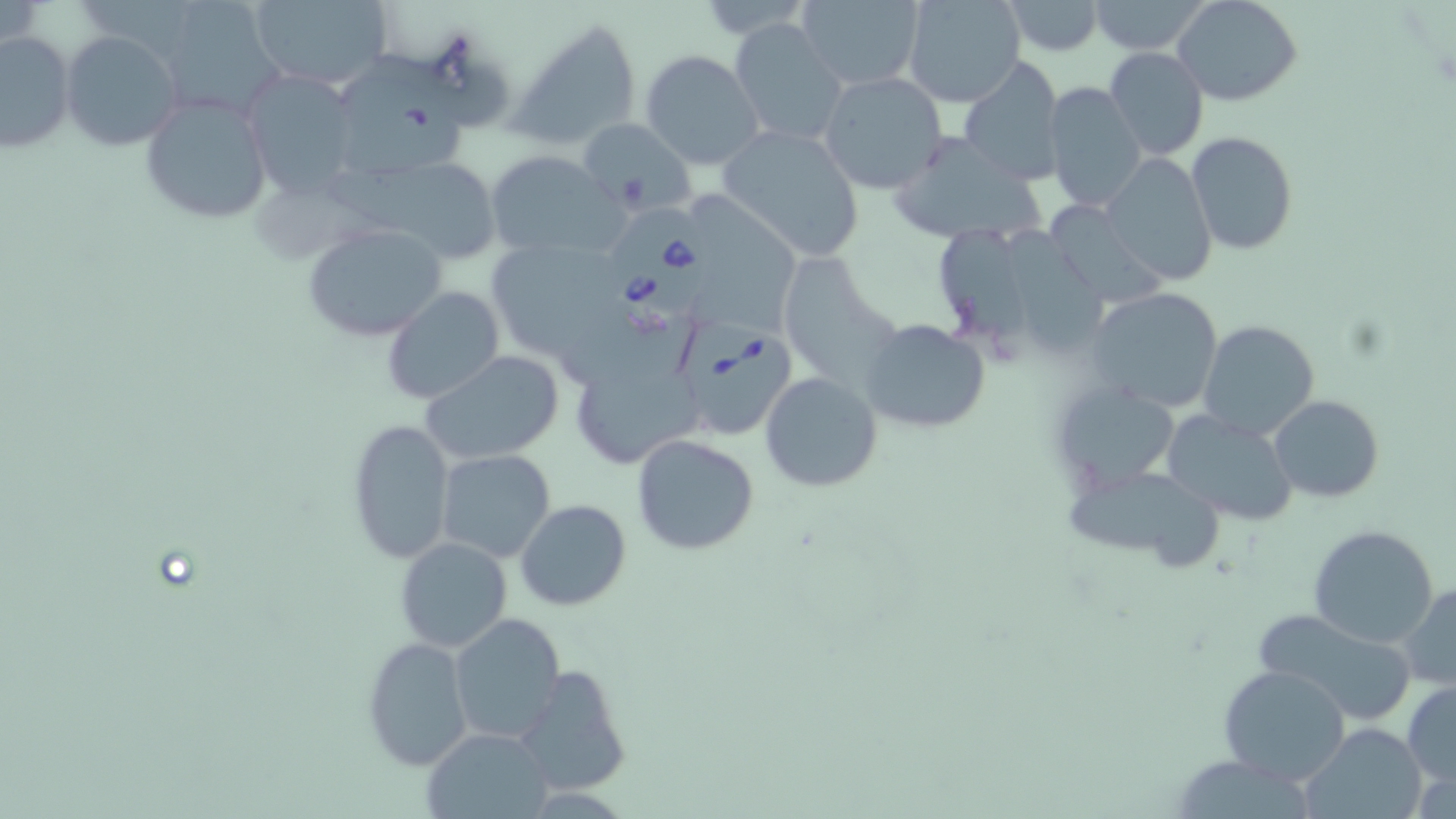

Approximate bounding boxes as [x1, y1, x2, y2] in pixels. Babesia divergens-infected red blood cell locations: [609, 205, 712, 324], [675, 325, 798, 445]. Uninfected red blood cell locations: [246, 0, 395, 92], [698, 0, 811, 37], [793, 0, 926, 90], [902, 0, 1028, 108], [1002, 0, 1106, 55], [1085, 0, 1213, 55], [1174, 0, 1303, 106], [169, 1, 286, 114], [508, 16, 643, 153], [729, 18, 848, 151], [61, 30, 180, 153], [0, 31, 75, 154], [1103, 47, 1210, 162], [640, 48, 765, 169], [335, 54, 471, 180], [957, 56, 1065, 187], [240, 68, 363, 200], [818, 70, 949, 193], [1045, 81, 1148, 217], [140, 94, 273, 225], [576, 116, 696, 217], [717, 124, 865, 262], [885, 131, 1048, 247], [1186, 131, 1297, 256], [485, 150, 624, 262], [1101, 151, 1218, 286], [326, 156, 499, 261], [694, 191, 811, 341], [1051, 205, 1167, 308], [301, 222, 449, 343], [1006, 222, 1113, 357], [939, 228, 1033, 358], [484, 236, 634, 351], [783, 250, 904, 390], [382, 285, 505, 406], [1088, 287, 1223, 412], [860, 318, 990, 435], [1199, 319, 1321, 442], [567, 341, 707, 470], [422, 351, 564, 464], [761, 372, 883, 492], [1049, 377, 1181, 498], [1269, 394, 1385, 504], [1161, 411, 1300, 526], [346, 418, 455, 564], [632, 433, 760, 556], [436, 450, 557, 563], [1062, 461, 1231, 578], [517, 500, 631, 611], [1306, 524, 1439, 648], [395, 537, 512, 652], [1400, 580, 1456, 688], [1247, 606, 1420, 726], [448, 613, 564, 744], [386, 618, 532, 757], [362, 637, 473, 769], [513, 663, 630, 796], [1218, 664, 1352, 784], [1402, 681, 1456, 789], [1300, 723, 1430, 819], [424, 728, 549, 817]. Slide-level diagnosis: Babesia divergens. Captured at 1000x magnification. Thin blood film. May-Grünwald-Giemsa-stained preparation. Single field of view. Image is 1456×819 pixels. Light microscopy.